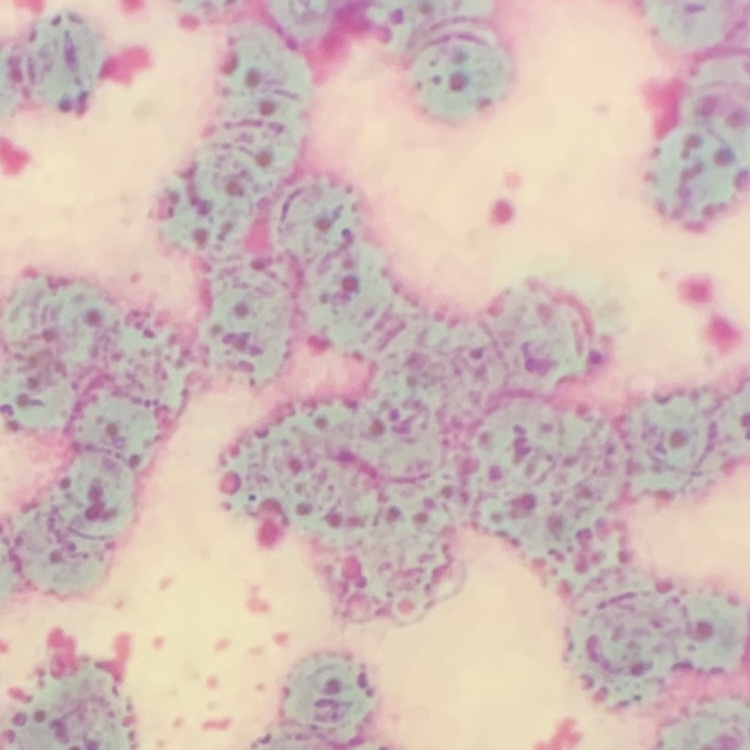

erythrocyte morphology = rouleaux formation
preparation = thin blood film
image type = square crop of a larger photomicrograph
stain = Field's or Giemsa